Locate every blood parasite and identify its species.
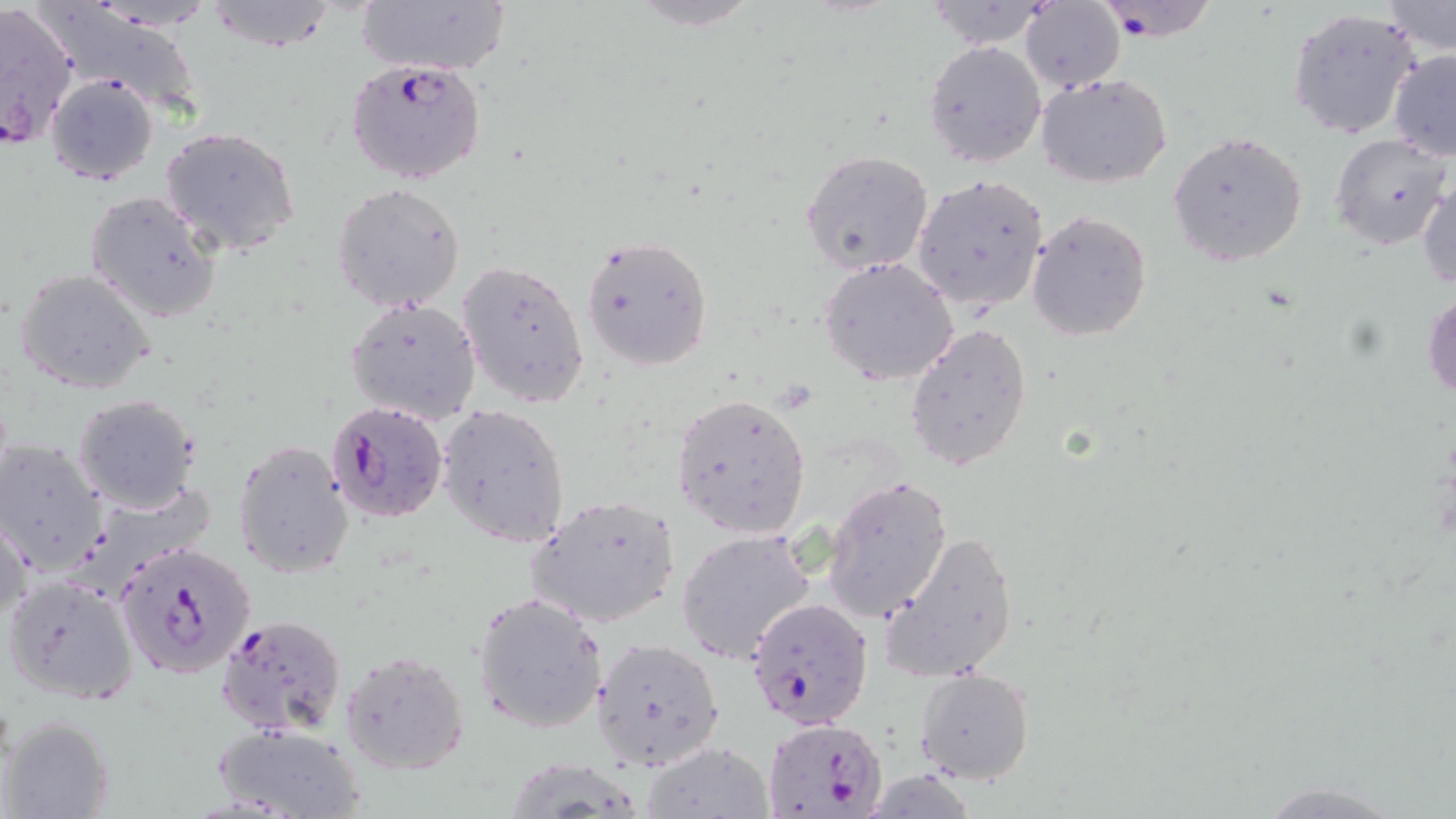
Approximate bounding boxes as (x1,y1)-(x2,y2) corner pairs in pixels.
Plasmodium falciparum-infected red blood cells: (1091,0)-(1219,41), (0,1)-(79,150), (346,59)-(487,185), (324,399)-(447,524), (116,538)-(259,679), (747,597)-(877,730), (214,613)-(346,737), (761,718)-(889,818).
No Plasmodium ovale, Plasmodium malariae, Plasmodium vivax, Babesia divergens, or Trypanosoma brucei observed.

Summary:
  - Uninfected red blood cell locations: (204,0)-(340,52), (356,0)-(511,78), (622,0)-(765,30), (923,0)-(1060,51), (1383,1)-(1455,55), (1021,3)-(1125,91), (1287,5)-(1421,140), (923,40)-(1046,169), (1388,50)-(1456,161), (1035,71)-(1173,189), (46,73)-(159,187), (159,126)-(301,256), (1168,130)-(1309,267), (1331,134)-(1454,252), (800,149)-(936,275), (911,174)-(1048,313), (1417,179)-(1456,293), (331,183)-(466,313), (84,190)-(223,324), (1025,209)-(1151,342), (579,234)-(714,371), (818,256)-(959,386), (456,257)-(590,409), (14,268)-(157,395), (1422,288)-(1456,405), (345,295)-(481,426), (904,324)-(1034,474), (671,391)-(812,538), (72,394)-(200,512), (437,403)-(571,548), (233,438)-(355,580), (0,440)-(107,573), (822,476)-(952,623), (526,496)-(681,629), (1,512)-(32,627), (878,527)-(1020,682), (676,529)-(815,665), (3,576)-(138,704), (470,592)-(607,734), (591,635)-(727,773), (339,648)-(473,776), (916,668)-(1034,785), (2,715)-(115,819), (208,719)-(366,819), (645,743)-(770,817), (1244,780)-(1421,817)
  - Slide-level diagnosis: Plasmodium falciparum
  - Preparation: thin blood film
  - Image size: 1456×819 pixels
  - Field of view: one of a larger specimen
  - Stain: May-Grünwald-Giemsa
  - Modality: optical microscopy
  - Magnification: 1000x